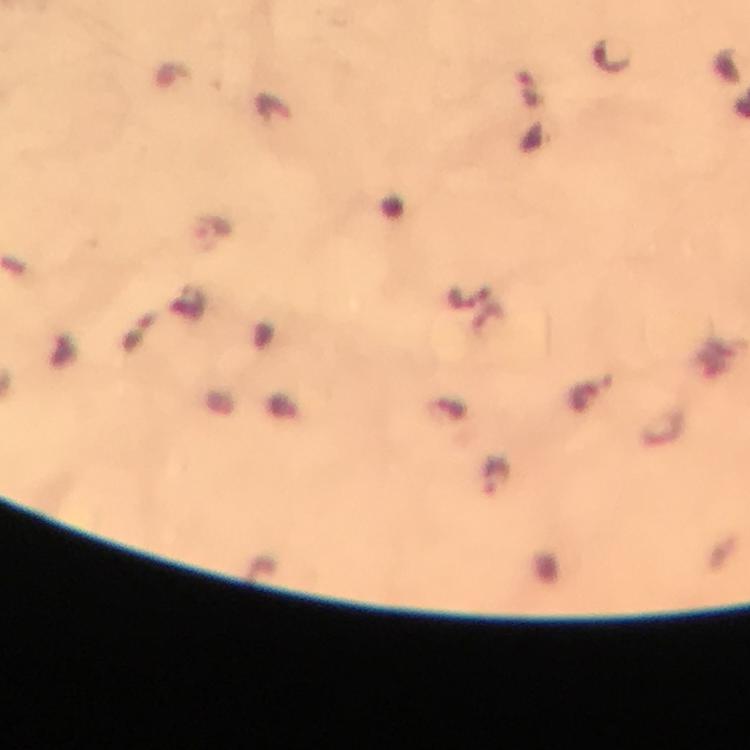

stain: Giemsa
preparation: thick smear
context: from a malaria diagnostic workup
magnification: 100x
immersion_oil: applied
capture: smartphone photograph through a microscope
cropped_from: a single field of view
malaria_parasite_locations: 'approximate object centers, in pixels from the top-left corner: (x=611, y=54), (x=212, y=231), (x=460, y=299), (x=585, y=396), (x=498, y=478)'
image_size: 750×750 pixels